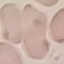 Malaria status: uninfected. Giemsa-stained preparation. Thin smear of blood. Acquired by smartphone through the microscope eyepiece. Cell patch, automatically extracted from a larger field of view and resized to 64 × 64 pixels.